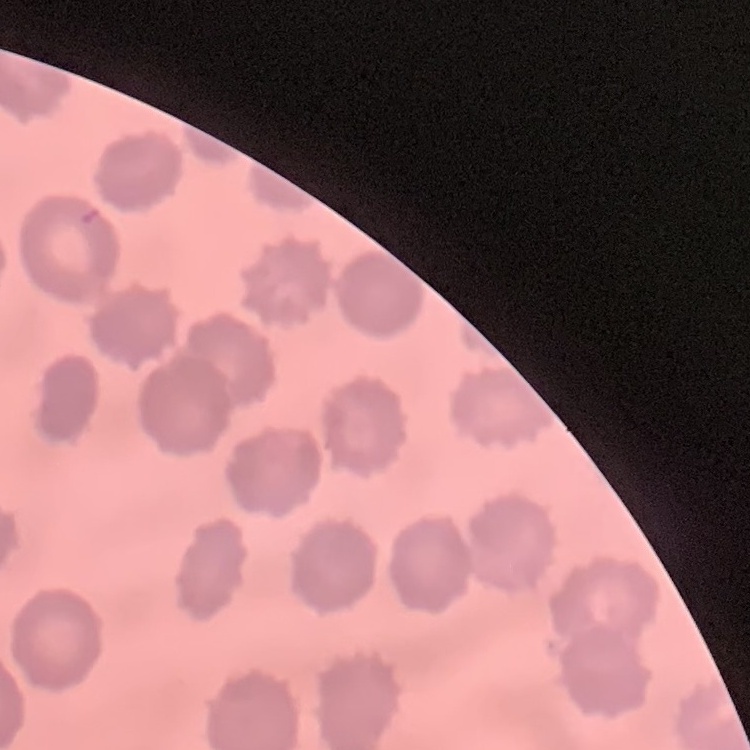
The red blood cells show no rouleaux formation. Thin blood film. Stained with either Field's or Giemsa. One tile cut from a larger photomicrograph.